Mark where cells are.
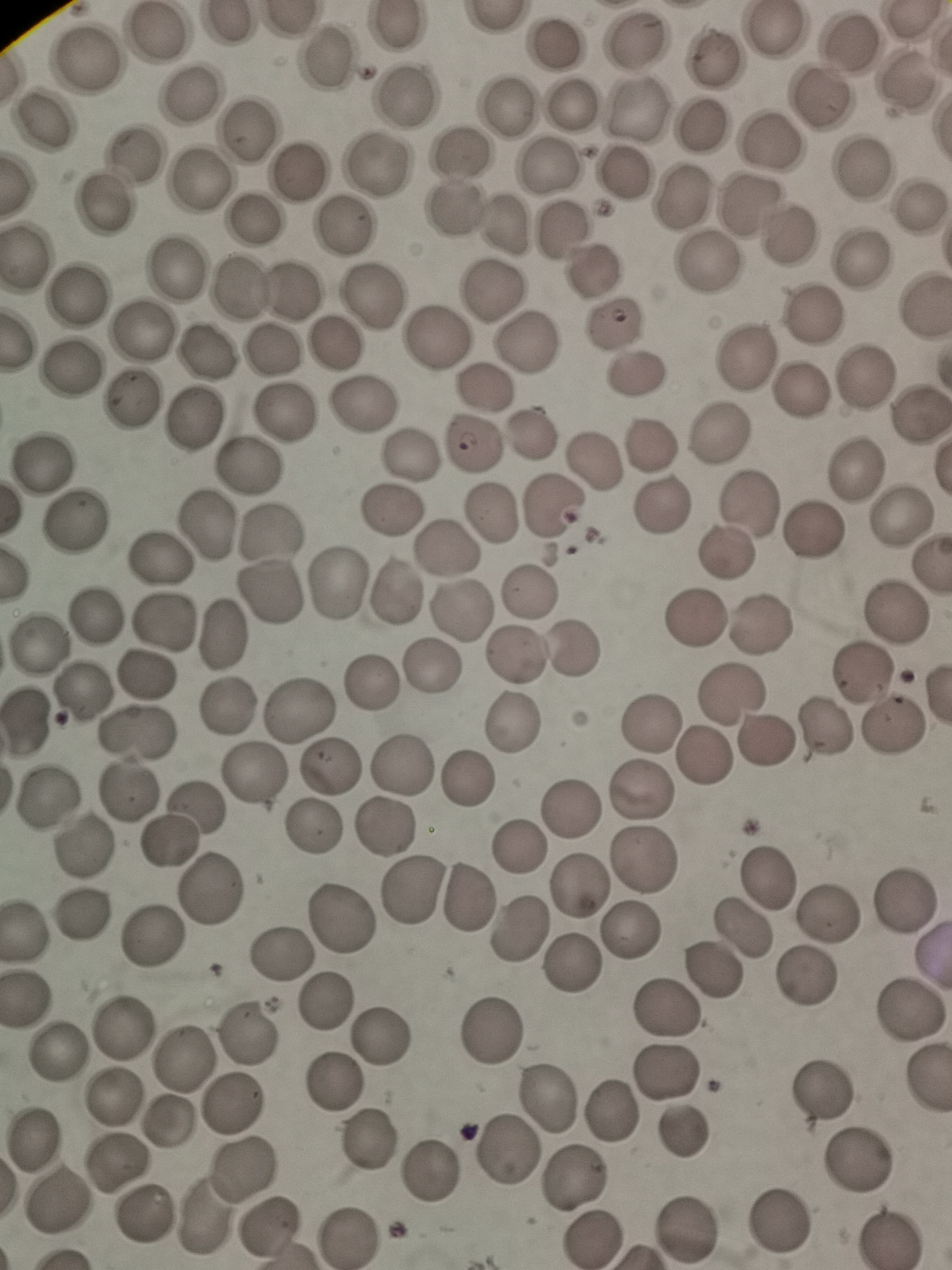
Approximate centers as {x, y} in pixels.
Cells: {395, 25}, {766, 32}, {159, 35}, {632, 41}, {557, 44}, {846, 44}, {86, 57}, {713, 57}, {327, 60}, {906, 80}, {406, 93}, {190, 94}, {817, 102}, {570, 105}, {508, 109}, {636, 110}, {42, 120}, {702, 123}, {251, 130}, {769, 143}, {132, 154}, {457, 154}, {374, 165}, {545, 168}, {859, 171}, {296, 174}, {628, 174}, {202, 180}, {680, 195}, {918, 201}, {100, 204}, {744, 205}, {455, 209}, {256, 220}, {342, 227}, {507, 228}, {562, 229}, {786, 238}, {28, 252}, {859, 257}, {708, 264}, {174, 265}, {592, 267}, {238, 286}, {490, 286}, {288, 287}, {82, 292}, {371, 293}, {924, 309}, {812, 314}, {612, 322}, {141, 331}, {437, 336}, {334, 341}, {525, 342}, {272, 347}, {208, 352}, {749, 353}, {72, 368}, {636, 368}, {867, 375}, {485, 386}, {802, 390}, {364, 401}, {134, 402}, {285, 411}, {919, 412}, {194, 423}, {716, 433}, {531, 436}, {475, 442}, {647, 443}, {410, 451}, {594, 461}, {43, 462}, {249, 464}, {856, 474}, {749, 501}, {394, 506}, {552, 507}, {661, 507}, {492, 513}, {898, 518}, {76, 523}, {210, 523}, {815, 528}, {273, 529}, {446, 550}, {729, 553}, {159, 556}, {930, 565}, {341, 580}, {396, 591}, {528, 593}, {273, 596}, {461, 610}, {892, 613}, {101, 614}, {161, 620}, {693, 622}, {762, 623}, {224, 634}, {43, 643}, {576, 644}, {518, 655}, {430, 667}, {148, 673}, {863, 674}, {369, 683}, {83, 690}, {733, 692}, {229, 704}, {297, 707}, {29, 722}, {515, 722}, {651, 725}, {822, 727}, {891, 727}, {139, 733}, {762, 743}, {703, 758}, {330, 761}, {402, 765}, {255, 771}, {467, 779}, {128, 790}, {642, 791}, {48, 798}, {198, 804}, {569, 808}, {314, 823}, {383, 828}, {173, 841}, {80, 848}, {516, 849}, {643, 857}, {770, 875}, {581, 885}, {413, 887}, {210, 888}, {470, 897}, {906, 901}, {828, 910}, {79, 915}, {340, 917}, {741, 927}, {519, 930}, {21, 931}, {154, 934}, {633, 934}, {279, 953}, {569, 966}, {706, 968}, {800, 979}, {23, 995}, {327, 999}, {668, 1010}, {913, 1014}, {494, 1027}, {121, 1028}, {243, 1029}, {386, 1035}, {57, 1049}, {185, 1056}, {665, 1070}, {333, 1086}, {551, 1093}, {118, 1094}, {817, 1096}, {233, 1104}, {612, 1107}, {168, 1127}, {688, 1131}, {34, 1134}, {371, 1139}, {508, 1149}, {117, 1162}, {859, 1163}, {244, 1169}, {425, 1175}, {572, 1176}, {58, 1200}, {143, 1216}, {779, 1221}, {690, 1225}, {269, 1227}, {889, 1235}, {593, 1236}, {351, 1239}.

Summary:
  - Preparation: thin blood film
  - Capture: smartphone camera at the microscope eyepiece
  - Image size: 952×1270 pixels
  - Stain: Giemsa
  - Field of view: single